Identify the parasite.
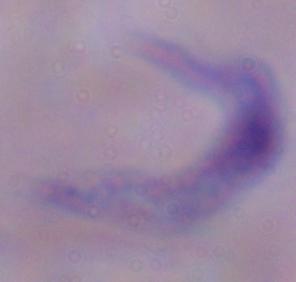

A trypanosome.

1000x magnification. Photomicrograph.